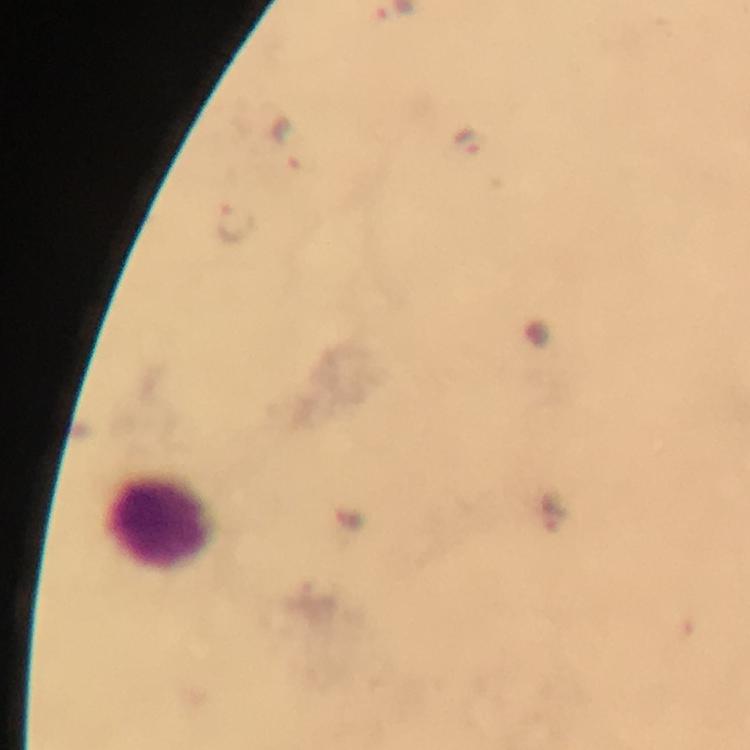

Approximate object centers, in pixels from the top-left corner.
Summary:
  - Malaria parasite locations: (x=287, y=138), (x=471, y=141), (x=237, y=223)
  - Leukocyte locations: (x=157, y=520)
  - Image size: 750×750 pixels
  - Stain: Giemsa
  - Capture: smartphone mounted on the microscope
  - Preparation: thick blood smear
  - Cropped from: one field of view
  - Immersion oil: applied
  - Magnification: 100x
  - Context: from a malaria diagnostic workup